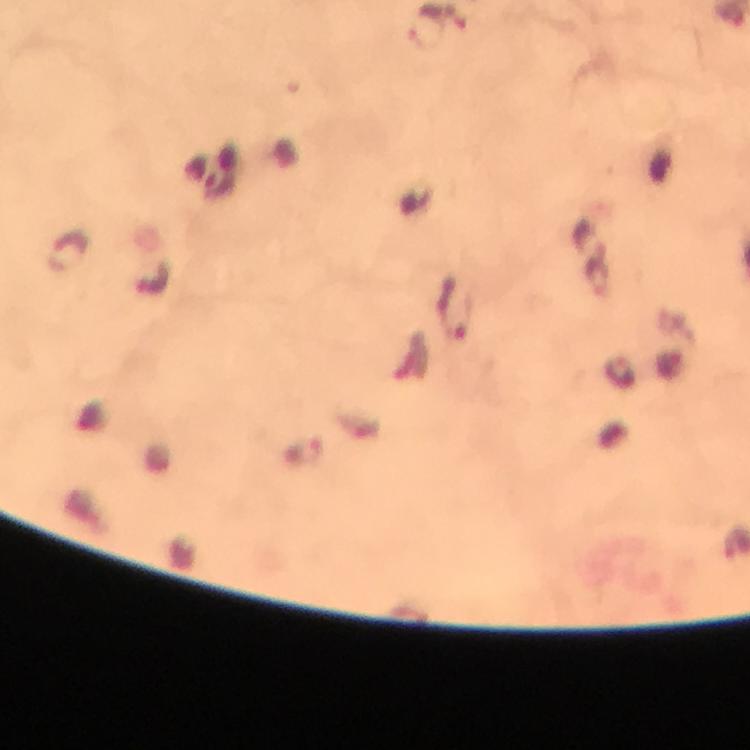

Approximate centers as (x, y) in pixels.
Summary:
  - Malaria parasite locations: (427, 29), (69, 251), (153, 278), (454, 308), (307, 453)
  - Image size: 750×750 pixels
  - Magnification: 100x
  - Context: from a malaria diagnostic workup
  - Capture: smartphone camera through the microscope
  - Stain: Giemsa
  - Immersion oil: used
  - Preparation: thick blood film
  - Cropped from: one field of view